Classify this cell by malaria status.
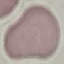
Uninfected.

Summary:
  - Image type: automatically extracted cell patch, resized to 64 × 64 pixels
  - Stain: Giemsa
  - Preparation: thin smear
  - Capture: smartphone camera at the microscope eyepiece